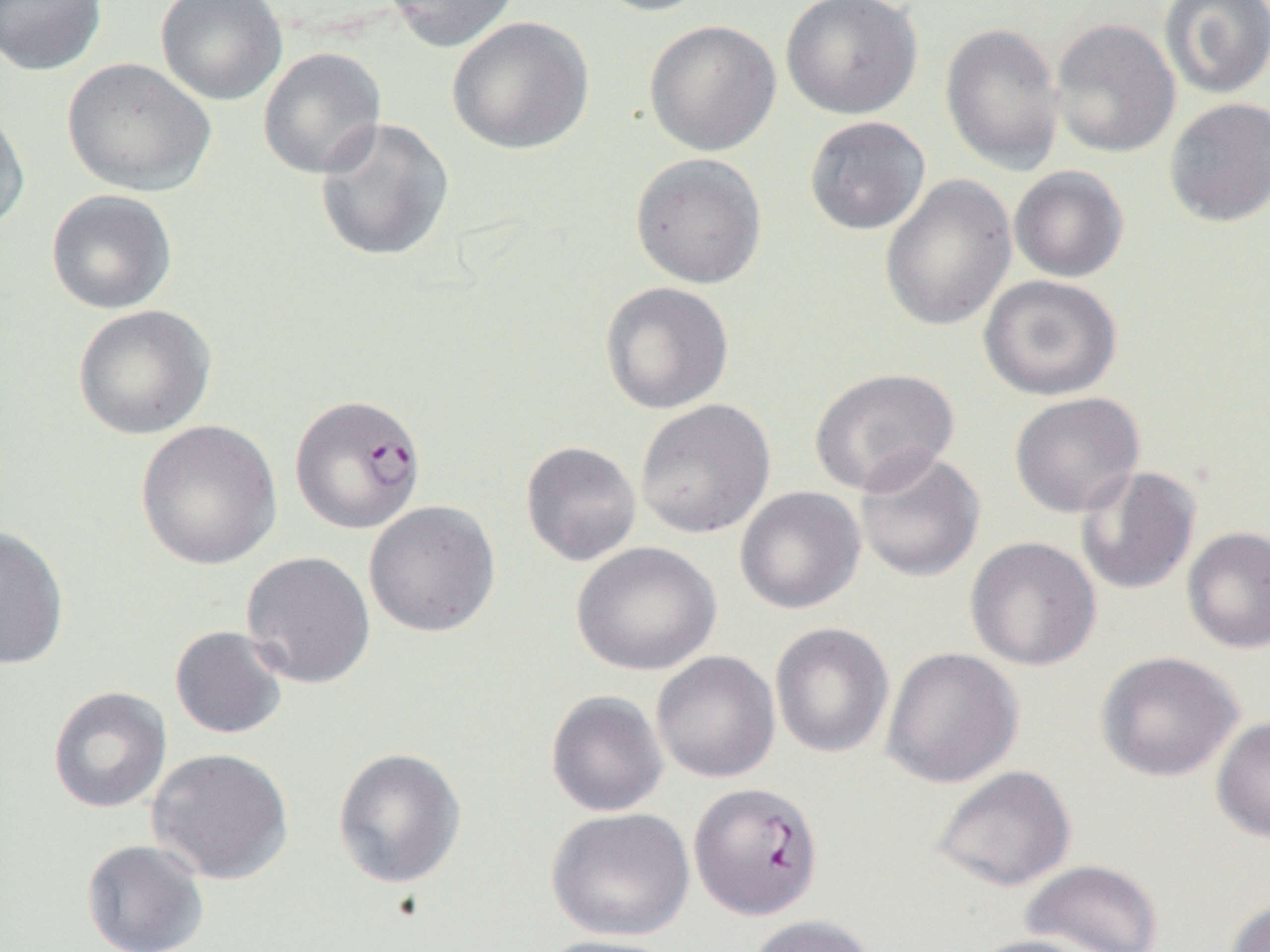

Summary:
  - Coordinate format: approximate bounding boxes as (x1,y1)-(x2,y2) corner pairs in pixels
  - Plasmodium falciparum-infected red blood cell locations: (289,392)-(427,535), (690,781)-(824,919)
  - Uninfected red blood cell locations: (0,0)-(107,76), (155,0)-(287,105), (383,0)-(521,52), (589,0)-(718,17), (781,0)-(923,120), (1159,0)-(1270,99), (447,16)-(594,155), (1050,18)-(1181,158), (644,19)-(782,156), (940,22)-(1065,175), (257,47)-(387,180), (62,58)-(215,196), (1164,97)-(1270,227), (0,105)-(31,236), (804,116)-(930,236), (313,117)-(455,262), (631,152)-(767,289), (1009,166)-(1129,283), (879,174)-(1018,332), (46,189)-(177,314), (978,274)-(1123,400), (599,281)-(734,414), (72,304)-(216,440), (809,367)-(959,496), (1009,392)-(1145,518), (635,399)-(775,539), (135,419)-(283,570), (520,440)-(642,566), (853,449)-(986,583), (1074,465)-(1201,596), (734,486)-(866,615), (364,500)-(501,637), (0,525)-(70,670), (1182,526)-(1270,653), (965,536)-(1101,671), (571,541)-(721,676), (241,551)-(376,689), (770,622)-(894,759), (169,625)-(289,740), (881,647)-(1024,788), (651,651)-(780,783), (1095,651)-(1244,782), (47,686)-(172,813), (546,690)-(669,817), (1211,716)-(1270,843), (147,747)-(295,885), (332,747)-(467,889), (931,765)-(1077,892), (546,807)-(695,941), (81,838)-(210,951), (1019,859)-(1164,952), (1223,896)-(1270,952), (746,914)-(878,952), (964,933)-(1102,952), (534,934)-(681,952)
  - Slide-level diagnosis: Plasmodium falciparum
  - Field of view: single
  - Preparation: thin blood smear
  - Magnification: 1000x
  - Modality: light microscopy
  - Image size: 1270×952 pixels